Assess this cell for malaria.
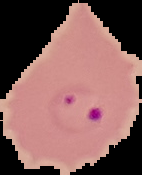

Parasitized.

{
  "image_type": "segmented cell region with the area outside set to black",
  "image_size": "142×175 pixels",
  "preparation": "thin blood smear"
}